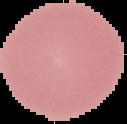
From a thin blood smear. Malaria status: uninfected. Image is 127×124 pixels. The area outside the segmented cell region is set to black.